Locate every leukocyte (white blood cell).
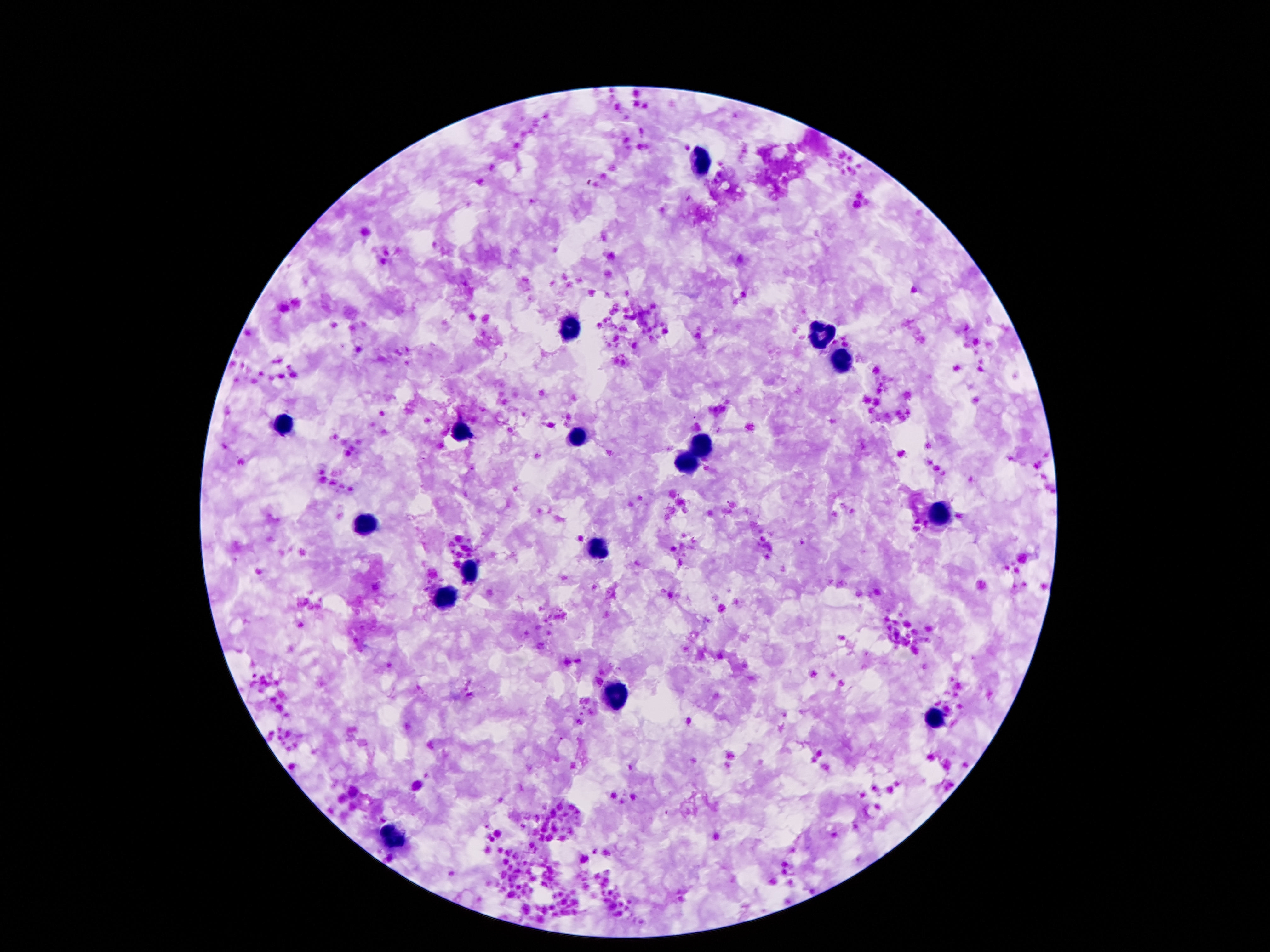
Approximate object centers, in pixels from the top-left corner.
Leukocytes: (x=700, y=159), (x=572, y=329), (x=814, y=335), (x=842, y=363), (x=284, y=423), (x=460, y=429), (x=578, y=439), (x=702, y=445), (x=686, y=465), (x=940, y=513), (x=362, y=527), (x=596, y=549), (x=466, y=573), (x=442, y=597), (x=614, y=691), (x=934, y=719), (x=392, y=841).

Summary:
  - Preparation: thick blood film
  - Image size: 1270×952 pixels
  - Capture: smartphone camera through the microscope eyepiece
  - Magnification: 100x
  - Patient malaria status: uninfected
  - Field of view: one from this slide
  - Stain: Giemsa